Identify the blood parasite species.
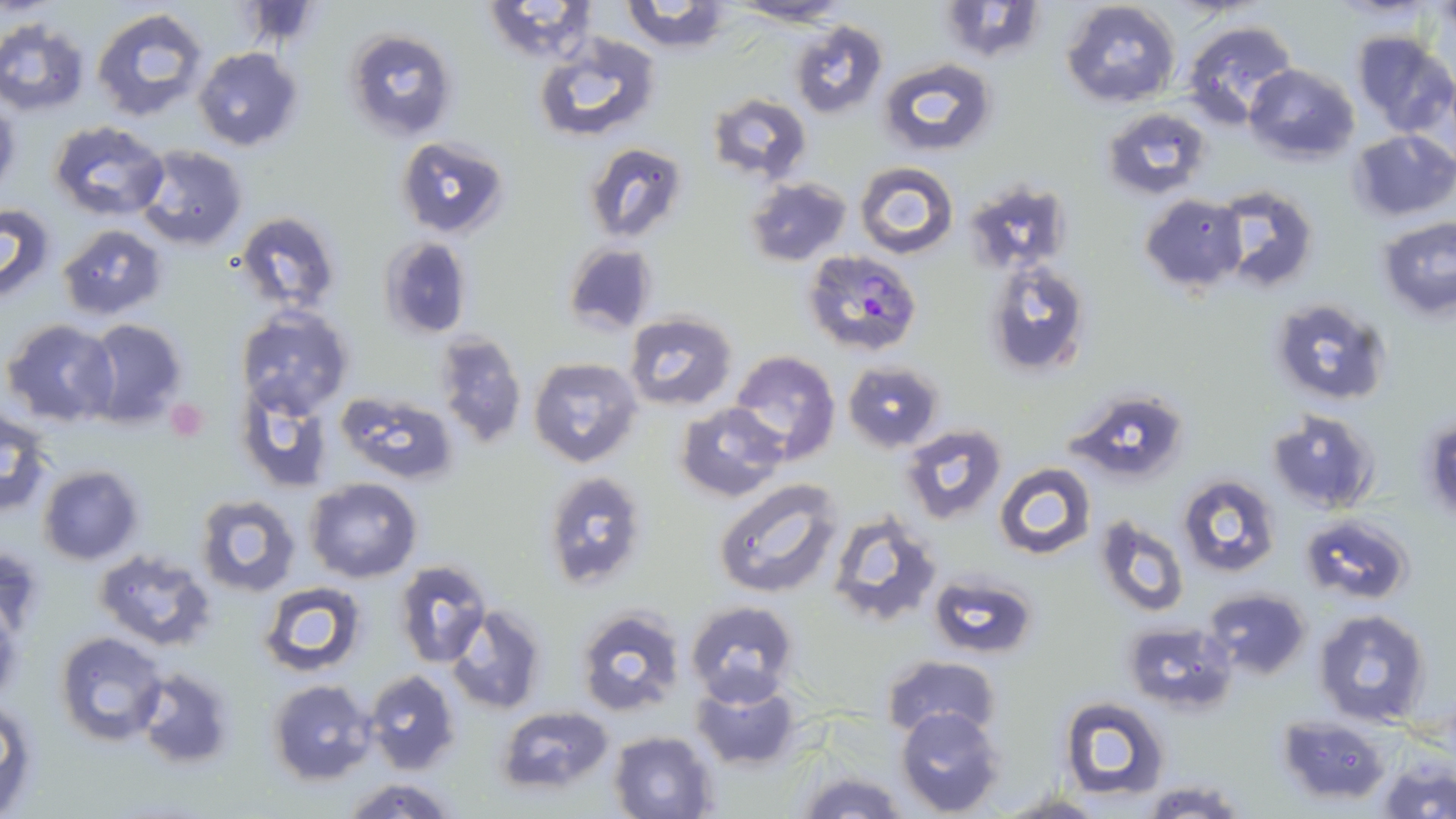

Plasmodium falciparum.

field of view = one of a larger specimen
Plasmodium falciparum-infected red blood cell locations = approximate bounding boxes as (x1, y1, x2, y2) in pixels: (802, 249, 923, 355)
magnification = 1000x
modality = optical microscopy
platelet locations = approximate bounding boxes as (x1, y1, x2, y2) in pixels: (165, 398, 209, 442)
stain = May-Grünwald-Giemsa
preparation = thin blood film
image size = 1456×819 pixels
uninfected red blood cell locations = approximate bounding boxes as (x1, y1, x2, y2) in pixels: (481, 0, 601, 64), (933, 0, 1046, 62), (1060, 0, 1181, 107), (617, 1, 737, 53), (727, 1, 854, 27), (90, 7, 212, 125), (0, 18, 90, 116), (789, 19, 888, 118), (1183, 20, 1299, 129), (345, 28, 459, 143), (1351, 31, 1454, 135), (532, 34, 662, 145), (192, 46, 303, 151), (878, 58, 996, 157), (1243, 63, 1359, 165), (706, 93, 813, 182), (0, 99, 21, 197), (1103, 107, 1213, 199), (46, 120, 169, 222), (1350, 129, 1455, 221), (397, 136, 511, 237), (583, 142, 689, 241), (134, 144, 248, 252), (854, 162, 958, 259), (745, 177, 851, 266), (964, 179, 1076, 274), (1214, 185, 1318, 292), (1139, 193, 1249, 294), (0, 201, 56, 304), (233, 212, 342, 313), (1378, 218, 1455, 318), (59, 222, 169, 320), (379, 236, 471, 337), (564, 241, 659, 336), (983, 258, 1090, 377), (1270, 297, 1392, 406), (236, 308, 353, 420), (623, 311, 738, 412), (81, 319, 189, 428), (4, 320, 120, 426), (434, 331, 527, 451), (727, 349, 842, 465), (527, 356, 643, 468), (843, 360, 945, 452), (233, 383, 335, 492), (1061, 388, 1189, 486), (336, 390, 456, 484), (675, 402, 788, 501), (1, 408, 55, 518), (1267, 409, 1380, 514), (1422, 416, 1455, 523), (901, 423, 1007, 523), (994, 462, 1096, 561), (38, 465, 145, 565), (541, 469, 651, 616), (1178, 475, 1281, 577), (304, 477, 422, 583), (714, 477, 843, 598), (196, 494, 301, 596), (826, 510, 941, 627), (1300, 513, 1413, 604), (1093, 515, 1189, 619), (92, 548, 217, 651), (393, 560, 491, 667), (929, 574, 1039, 658), (259, 582, 369, 675), (1204, 587, 1311, 678), (685, 600, 798, 705), (443, 606, 547, 715), (574, 606, 687, 718), (1314, 609, 1433, 728), (1120, 620, 1236, 713), (56, 632, 168, 747), (882, 655, 1001, 741), (132, 668, 237, 770), (362, 669, 461, 775), (267, 679, 379, 786), (690, 681, 802, 770), (1060, 696, 1171, 803), (0, 699, 37, 815), (494, 704, 615, 798), (895, 707, 1005, 816), (1278, 715, 1392, 805), (608, 730, 720, 819), (1379, 761, 1456, 819), (793, 765, 909, 819), (338, 777, 461, 819), (1139, 781, 1252, 818), (997, 791, 1105, 819)